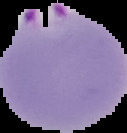
Summary:
  - Image size: 127×133 pixels
  - Result: Plasmodium parasites identified
  - Image type: segmented cell region on a black background
  - Preparation: thin blood smear